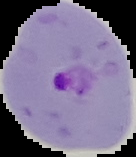

preparation: thin blood smear
image_type: segmented cell region on a black background
image_size: 136×157 pixels
result: malaria parasites detected